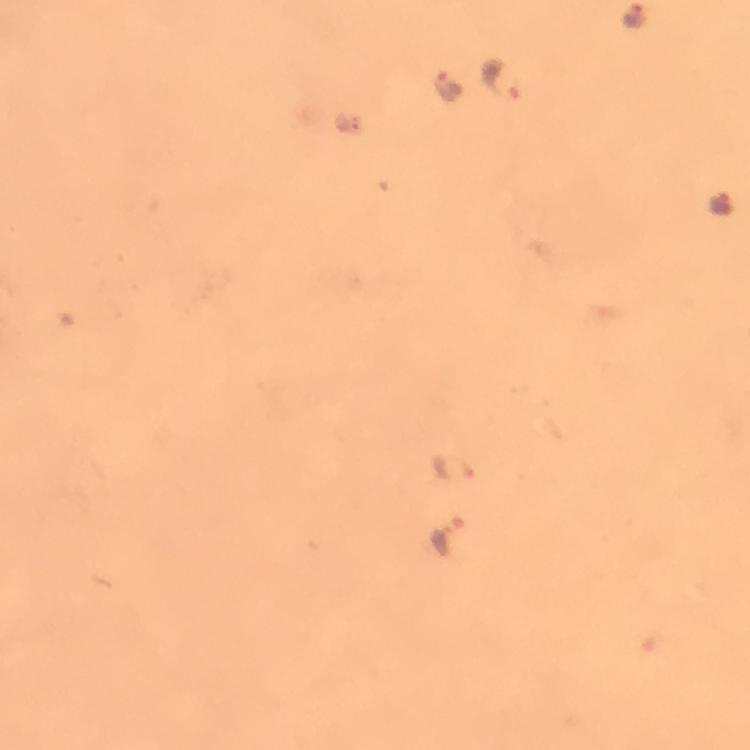

Approximate centers as [x, y] in pixels. Plasmodium parasite locations: [635, 17], [503, 78], [445, 84], [719, 205], [456, 465], [447, 537]. Image is 750×750 pixels. Immersion oil applied. Giemsa-stained preparation. From a diagnostic examination for malaria. Smartphone photograph taken through a microscope. Cropped region of a single field of view. 100x magnification. Thick smear.